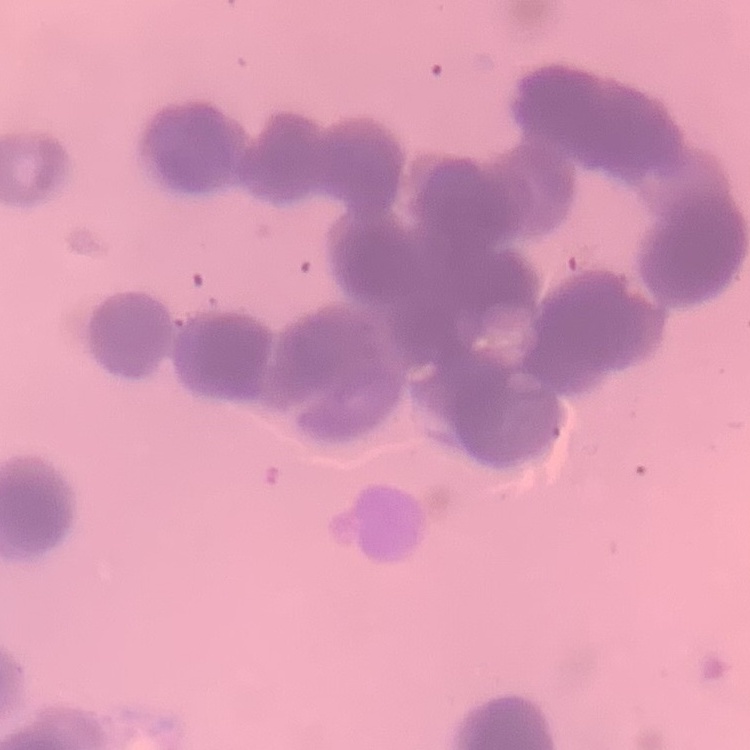
Summary:
  - Erythrocyte morphology: rouleaux formation
  - Preparation: thin blood smear
  - Stain: Field's or Giemsa
  - Image type: square crop of a larger photomicrograph